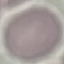

Result: negative for malaria parasites. Photographed with a smartphone camera at the microscope eyepiece. Thin blood film. Cell patch, automatically extracted from a larger field of view and resized to 64 × 64 pixels. Giemsa stain.